Look for Plasmodium parasites.
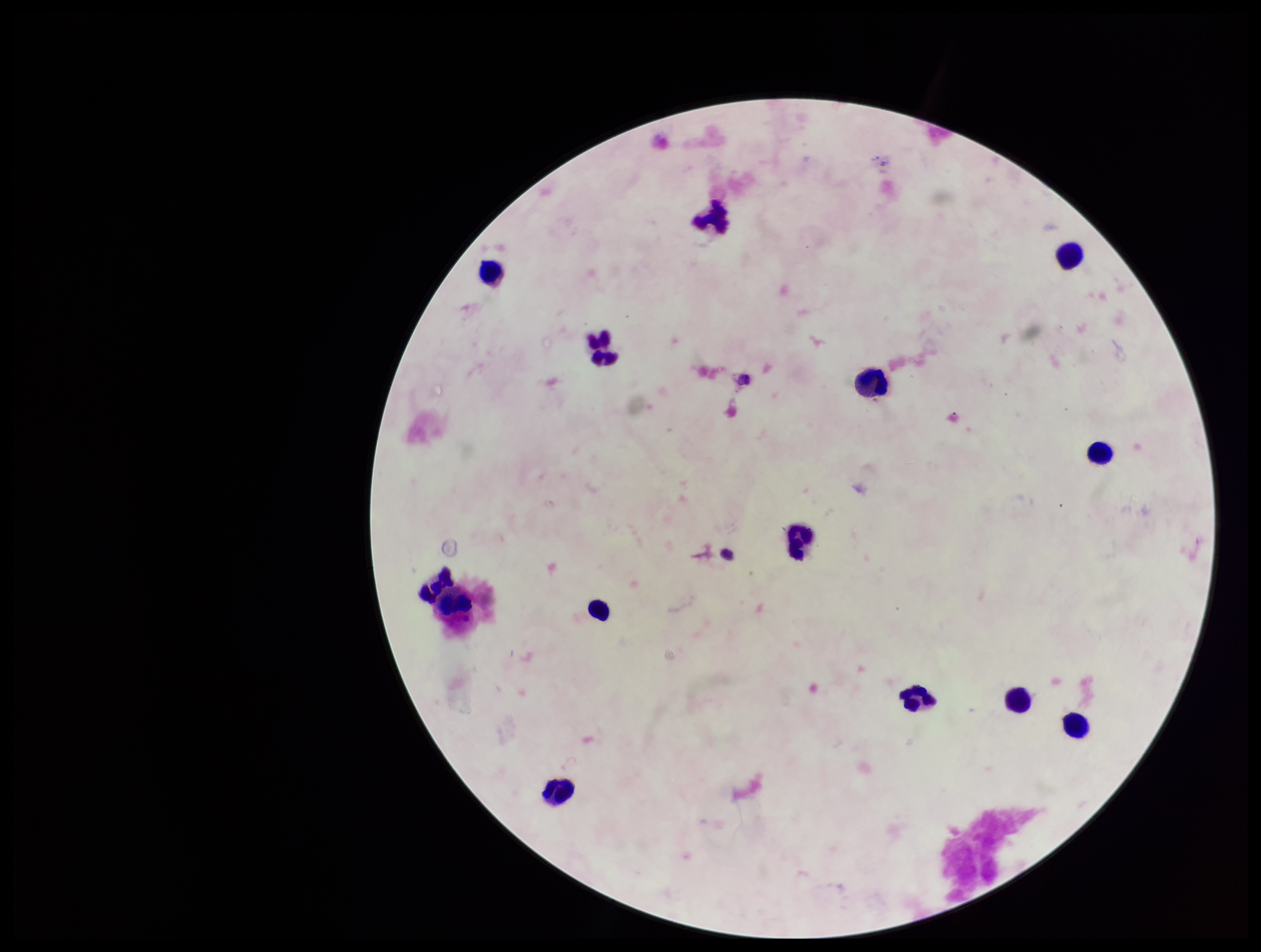

None seen.

Parasite count: 0. Preparation: thick blood smear. Smartphone photograph taken through the eyepiece of a microscope. Patient malaria status: negative. Leukocyte count: 14. Giemsa stain. Image is 1261×952 pixels. Single field of view.